Identify the blood parasite species.
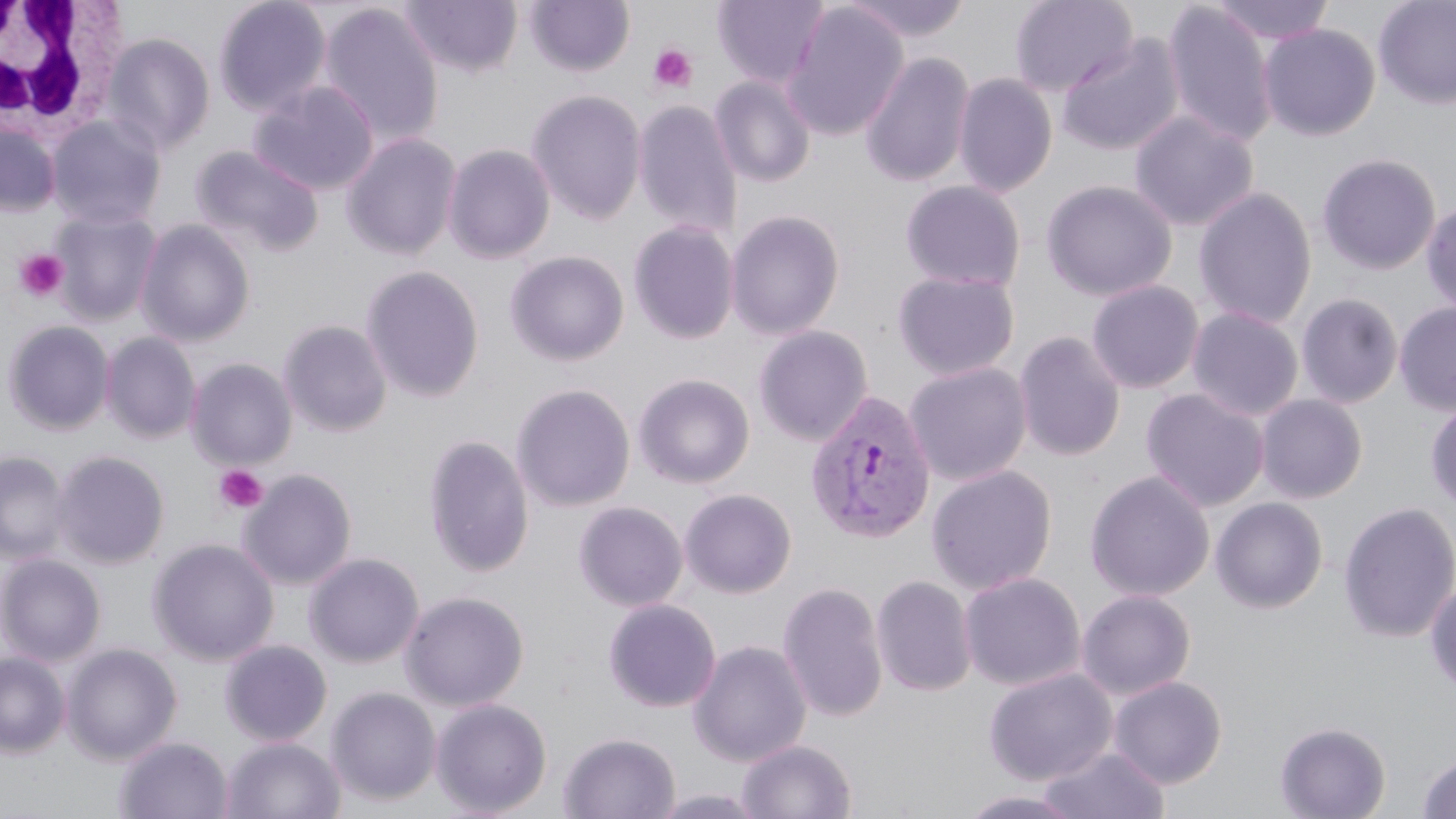
Plasmodium vivax.

{
  "image_size": "1456×819 pixels",
  "plasmodium_vivax_infected_red_blood_cell_locations": "approximate bounding boxes as (x1, y1, x2, y2) in pixels: (804, 390, 936, 544)",
  "magnification": "1000x",
  "uninfected_red_blood_cell_locations": "approximate bounding boxes as (x1, y1, x2, y2) in pixels: (213, 0, 332, 117), (399, 0, 522, 77), (525, 0, 635, 77), (712, 0, 830, 90), (842, 0, 973, 42), (1009, 0, 1138, 97), (1208, 0, 1336, 46), (1372, 0, 1456, 110), (1161, 2, 1278, 149), (781, 3, 909, 141), (319, 5, 444, 148), (1258, 23, 1380, 141), (102, 32, 215, 155), (1056, 34, 1185, 156), (860, 50, 975, 188), (953, 73, 1057, 198), (710, 75, 816, 188), (249, 81, 378, 196), (527, 89, 647, 226), (632, 99, 742, 241), (1130, 111, 1258, 231), (47, 115, 167, 229), (0, 122, 61, 216), (342, 132, 462, 260), (443, 143, 555, 264), (192, 145, 324, 257), (1317, 152, 1442, 275), (1041, 179, 1177, 301), (899, 180, 1026, 293), (1193, 186, 1318, 330), (1421, 200, 1456, 318), (50, 208, 162, 325), (726, 209, 845, 341), (136, 220, 255, 347), (628, 222, 740, 345), (505, 250, 629, 367), (361, 265, 485, 403), (892, 270, 1020, 381), (1087, 280, 1204, 393), (1296, 293, 1404, 409), (1394, 301, 1456, 415), (1187, 307, 1304, 422), (2, 319, 115, 435), (278, 320, 392, 437), (753, 325, 873, 447), (1013, 331, 1126, 462), (101, 332, 201, 444), (187, 358, 296, 471), (904, 362, 1032, 486), (634, 373, 755, 489), (511, 384, 636, 512), (1141, 388, 1270, 512), (1255, 394, 1368, 504), (1425, 398, 1456, 512), (424, 434, 534, 578), (52, 450, 169, 569), (0, 451, 70, 565), (926, 464, 1057, 595), (240, 469, 357, 590), (1085, 470, 1215, 601), (679, 488, 797, 599), (1210, 497, 1328, 613), (1338, 500, 1456, 643), (573, 501, 688, 612), (148, 538, 278, 666), (304, 552, 424, 668), (0, 554, 106, 666), (959, 571, 1086, 691), (871, 575, 977, 697), (1425, 578, 1456, 694), (777, 581, 888, 722), (1077, 589, 1196, 700), (400, 590, 530, 712), (603, 599, 721, 713), (688, 639, 812, 768), (220, 640, 332, 746), (61, 643, 182, 765), (0, 651, 70, 757), (984, 667, 1117, 786), (1108, 675, 1227, 788), (326, 686, 441, 807), (431, 698, 551, 817), (1275, 721, 1391, 819), (559, 731, 680, 819), (115, 736, 233, 818), (221, 736, 345, 819), (737, 738, 857, 818), (1035, 744, 1170, 818), (1417, 752, 1456, 819), (649, 788, 769, 819), (956, 789, 1089, 819)",
  "modality": "optical microscopy",
  "white_blood_cell_locations": "approximate bounding boxes as (x1, y1, x2, y2) in pixels: (1, 0, 126, 144)",
  "stain": "May-Grünwald-Giemsa",
  "field_of_view": "single",
  "platelet_locations": "approximate bounding boxes as (x1, y1, x2, y2) in pixels: (649, 44, 698, 93), (14, 248, 70, 303), (214, 465, 267, 516)",
  "preparation": "thin blood film"
}